Assess the morphology of the erythrocytes.
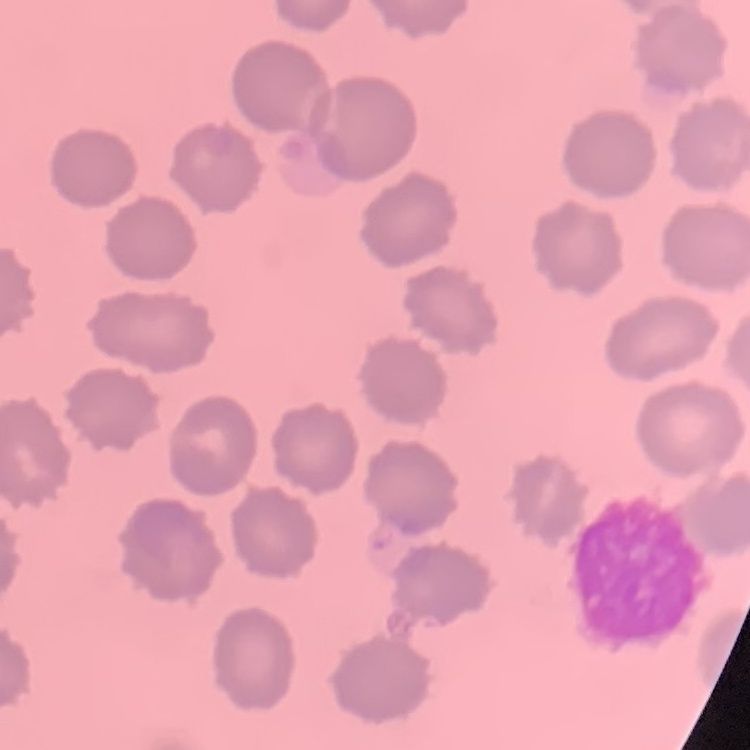

No rouleaux formation.

Thin blood smear. Stained with either Field's or Giemsa. One tile cut from a larger photomicrograph.